Point out each Plasmodium parasite.
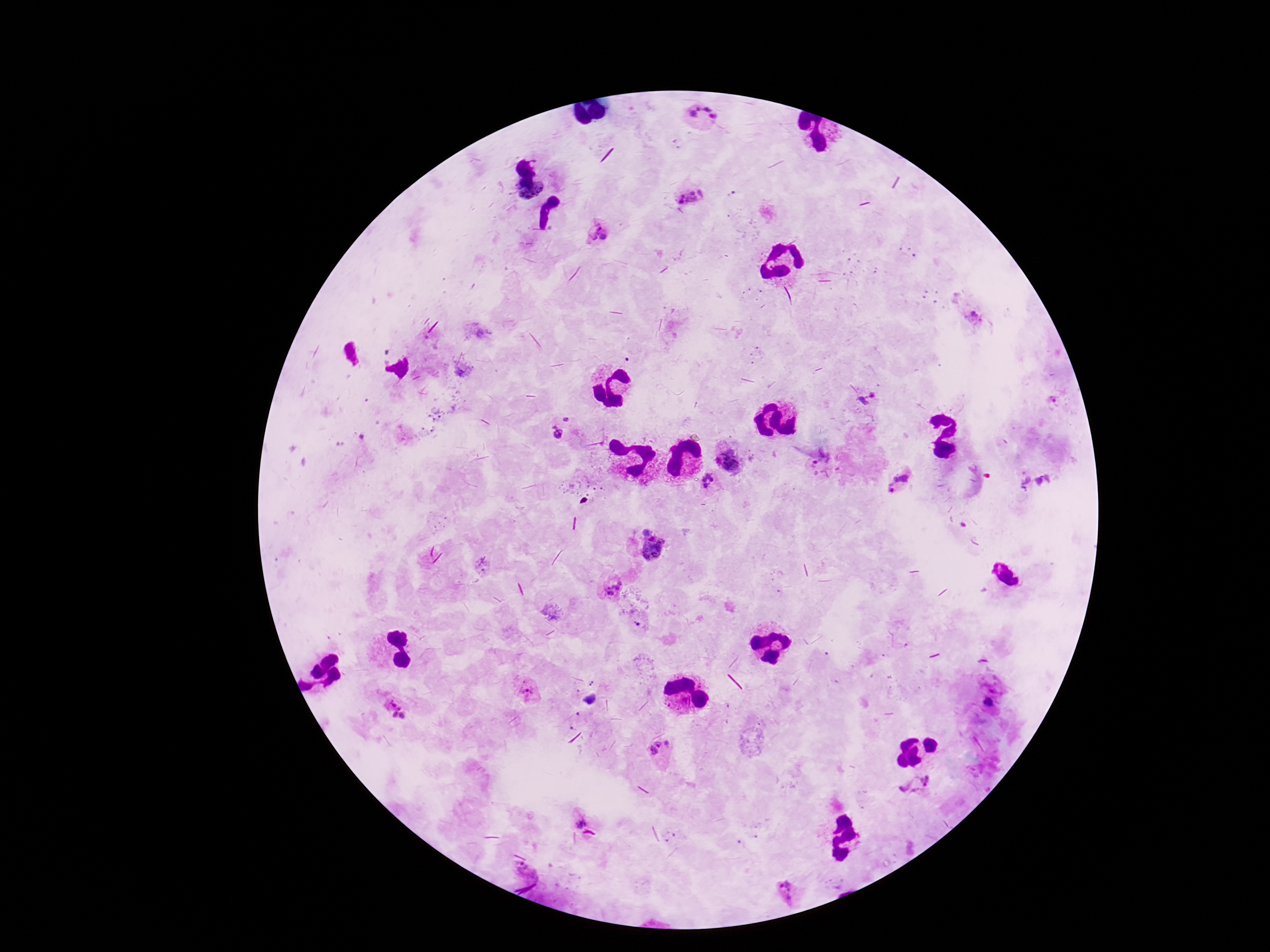

Approximate centers as {x, y} in pixels.
Plasmodium parasites: {704, 118}, {532, 192}, {690, 196}, {597, 233}, {868, 401}, {568, 417}, {555, 433}, {729, 462}, {821, 467}, {708, 483}, {901, 484}, {654, 551}, {611, 588}, {527, 692}, {657, 748}, {917, 784}, {581, 822}, {526, 869}, {787, 893}.

Giemsa stain. Smartphone photograph taken through the microscope eyepiece. Single field of view. Patient malaria status: positive. Image is 1270×952 pixels. 100x magnification. Thick peripheral-blood smear.